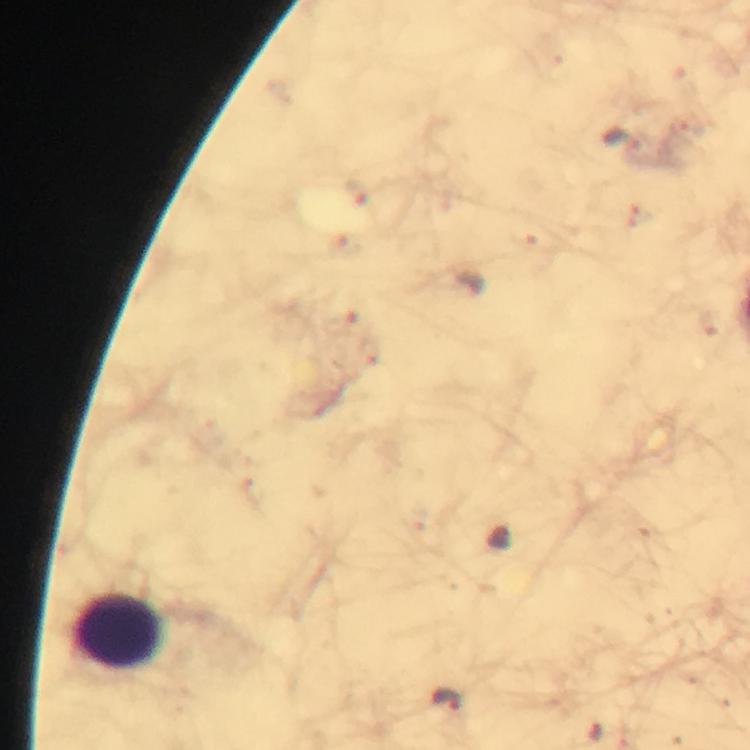
cropped from = a single field of view
context = from a malaria diagnostic workup
leukocyte locations = approximate object centers, in pixels from the top-left corner: (x=121, y=630)
image size = 750×750 pixels
immersion oil = applied
stain = Giemsa
capture = smartphone photograph through a microscope
preparation = thick smear
magnification = 100x
malaria parasite locations = approximate object centers, in pixels from the top-left corner: (x=620, y=140), (x=448, y=699)